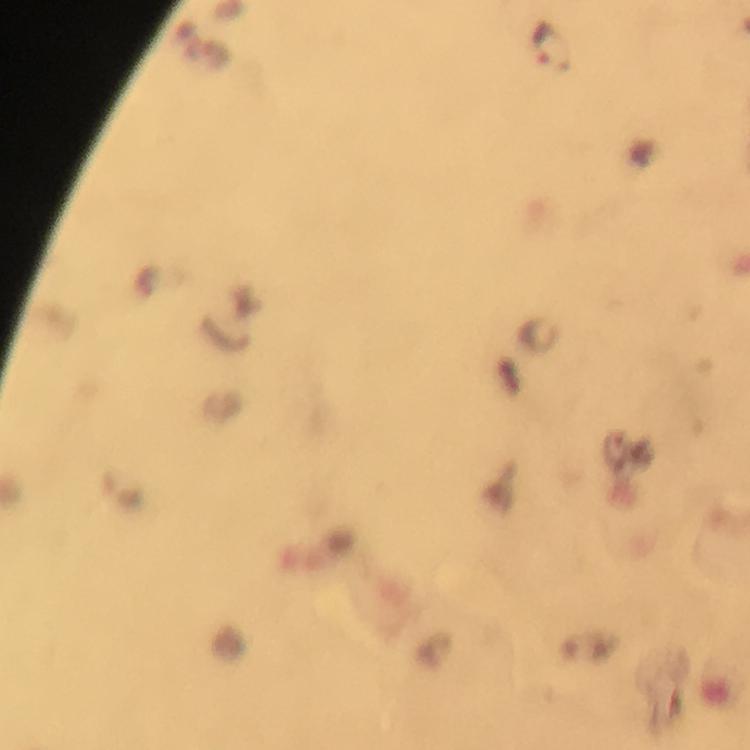
magnification = 100x
Plasmodium parasite locations = approximate centers as {x, y} in pixels: {551, 47}
stain = Giemsa
cropped from = a single field of view
context = from a diagnostic examination for malaria
immersion oil = used
capture = smartphone photograph through a microscope
preparation = thick blood smear
image size = 750×750 pixels